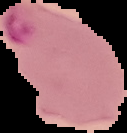

image size = 127×133 pixels
malaria status = parasitized
preparation = thin blood film
image type = segmented cell region on a black background